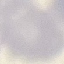

Summary:
  - Result: no malaria parasites detected
  - Capture: smartphone through the microscope eyepiece
  - Preparation: thin blood film
  - Image type: automatically extracted cell patch, resized to 64 × 64 pixels
  - Stain: Giemsa